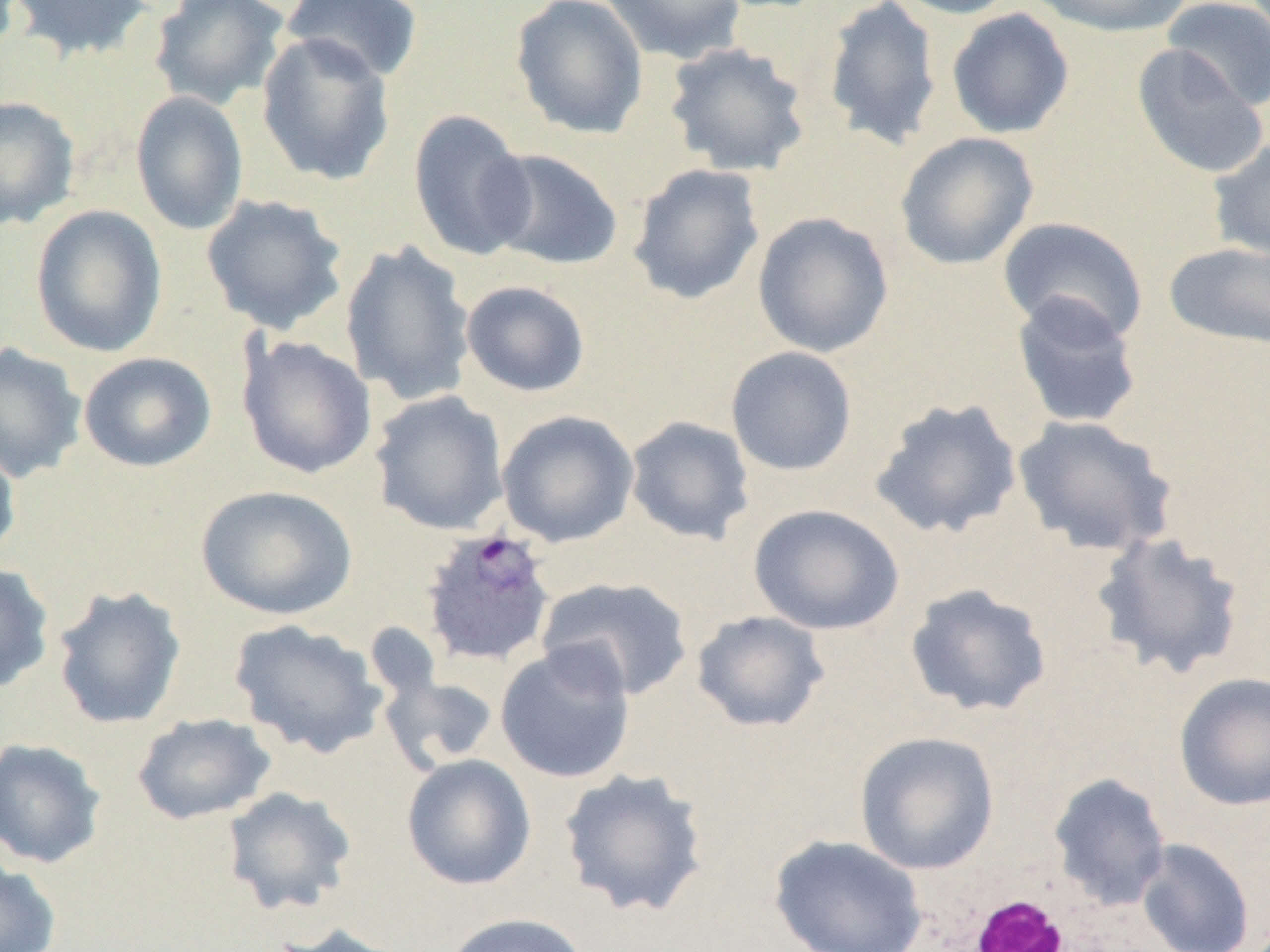 Approximate bounding boxes as (x1, y1, x2, y2) in pixels. White blood cell locations: (964, 893, 1074, 951). Uninfected red blood cell locations: (7, 0, 153, 62), (149, 0, 290, 111), (510, 0, 649, 140), (599, 0, 747, 64), (822, 0, 943, 150), (886, 0, 1023, 19), (1028, 0, 1192, 38), (1162, 0, 1270, 110), (282, 1, 423, 84), (946, 8, 1074, 139), (255, 31, 396, 187), (662, 41, 812, 177), (1131, 44, 1269, 181), (131, 90, 249, 235), (0, 96, 81, 231), (407, 109, 535, 262), (895, 132, 1040, 271), (1207, 137, 1270, 263), (483, 148, 624, 271), (627, 163, 766, 305), (200, 194, 349, 335), (30, 204, 167, 358), (751, 212, 894, 358), (997, 216, 1149, 342), (339, 240, 477, 407), (1163, 241, 1270, 351), (460, 279, 591, 397), (1009, 292, 1144, 431), (236, 336, 377, 479), (0, 342, 88, 484), (725, 346, 858, 476), (78, 352, 217, 472), (369, 391, 509, 535), (869, 397, 1023, 540), (497, 410, 640, 548), (625, 415, 755, 545), (1012, 415, 1178, 558), (0, 438, 21, 566), (195, 484, 358, 620), (748, 503, 904, 635), (1092, 531, 1247, 680), (0, 561, 55, 695), (536, 575, 694, 701), (904, 583, 1053, 718), (51, 585, 187, 729), (691, 610, 830, 733), (228, 619, 389, 759), (495, 641, 636, 784), (380, 672, 501, 772), (1173, 672, 1270, 811), (132, 712, 276, 825), (854, 731, 1000, 875), (0, 738, 107, 869), (401, 753, 537, 890), (557, 767, 710, 919), (1047, 772, 1172, 912), (221, 786, 358, 917), (769, 834, 927, 952), (1136, 838, 1255, 952), (0, 858, 62, 952), (439, 912, 592, 952), (267, 922, 412, 952). Plasmodium ovale-infected red blood cell locations: (419, 527, 556, 667). Slide-level diagnosis: Plasmodium ovale. One field of a larger specimen. Image is 1270×952 pixels. Captured at 1000x magnification. Thin blood smear. Light microscopy.